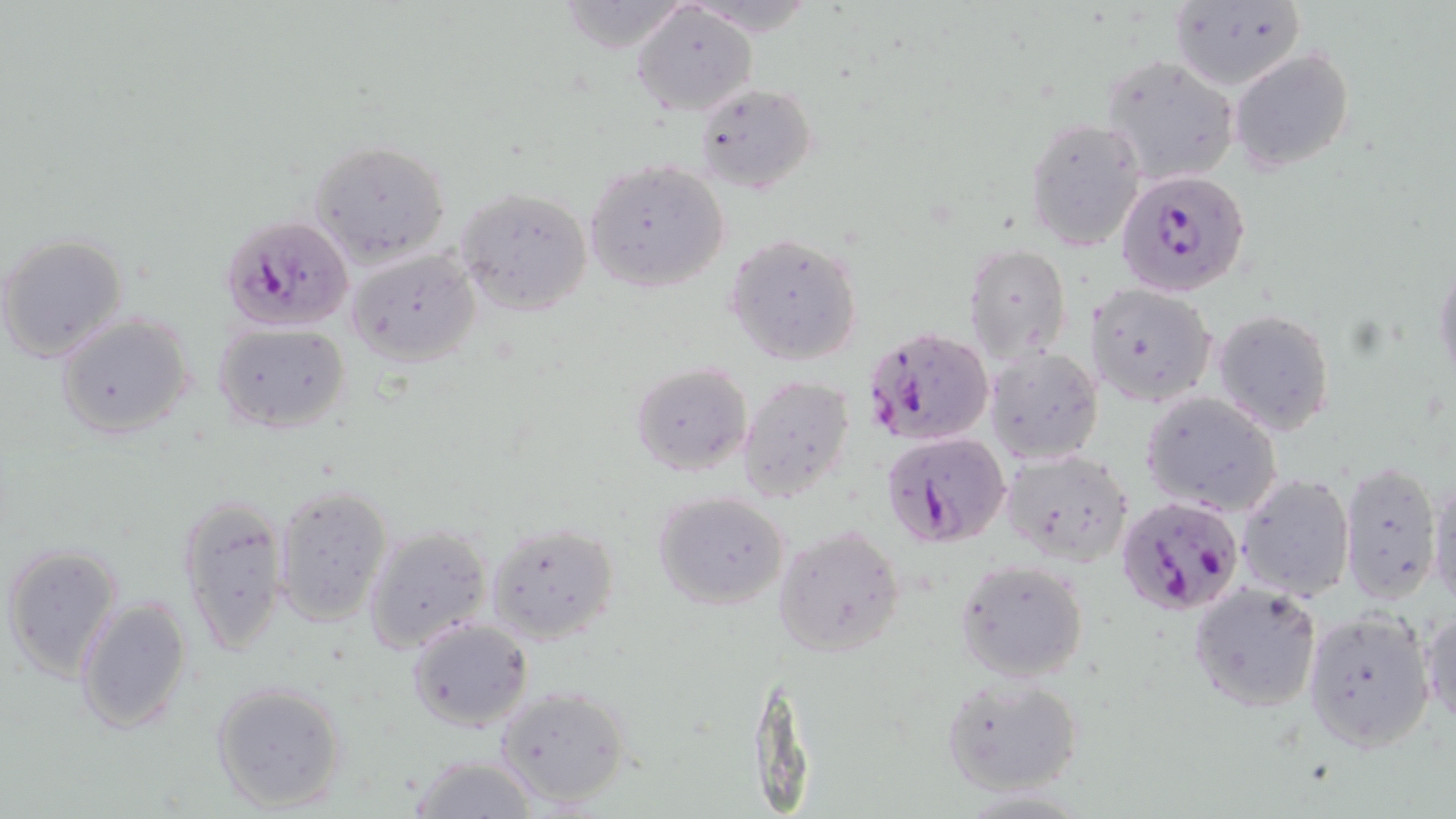
slide-level diagnosis = Plasmodium falciparum
field of view = one of a larger specimen
stain = May-Grünwald-Giemsa
uninfected red blood cell locations = approximate bounding boxes as (x1,y1)-(x2,y2) corner pairs in pixels: (1169,2)-(1304,92), (632,5)-(757,117), (1230,48)-(1355,173), (1101,54)-(1241,187), (693,83)-(816,195), (1023,117)-(1146,251), (310,138)-(452,269), (584,160)-(731,293), (456,185)-(593,315), (1,232)-(129,362), (726,235)-(863,366), (964,244)-(1070,365), (346,248)-(481,367), (1433,257)-(1456,389), (1086,283)-(1218,408), (1212,309)-(1336,437), (55,311)-(195,442), (212,322)-(353,434), (986,348)-(1104,464), (630,362)-(752,477), (737,375)-(854,502), (1140,392)-(1282,518), (1001,447)-(1136,566), (1338,460)-(1443,605), (1236,472)-(1357,603), (1427,474)-(1456,610), (272,484)-(393,624), (652,491)-(790,610), (179,494)-(289,655), (485,520)-(621,645), (364,524)-(493,652), (774,525)-(906,658), (0,542)-(124,682), (955,556)-(1090,683), (1187,582)-(1322,712), (76,596)-(191,735), (1421,606)-(1455,728), (1301,609)-(1437,753), (406,617)-(532,730), (941,674)-(1085,798), (210,680)-(349,815), (494,683)-(632,809), (409,754)-(539,819)
image size = 1456×819 pixels
Plasmodium falciparum-infected red blood cell locations = approximate bounding boxes as (x1,y1)-(x2,y2) corner pairs in pixels: (1121,170)-(1249,299), (218,216)-(353,334), (864,324)-(996,448), (880,431)-(1011,547), (1116,497)-(1244,616)
magnification = 1000x
modality = light microscopy
preparation = thin blood film